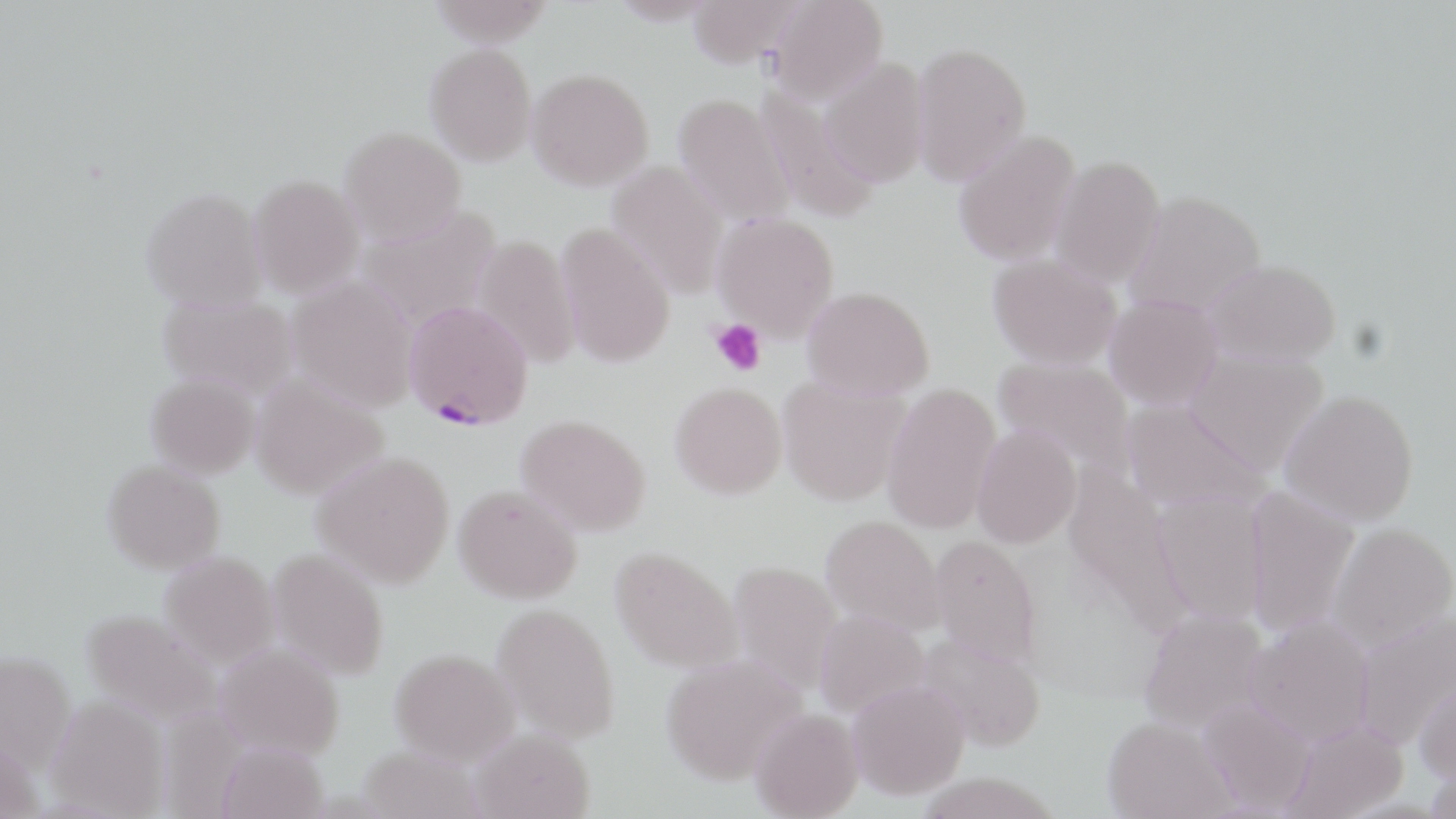 Approximate bounding boxes as [x1, y1, x2, y2] in pixels. Uninfected red blood cell locations: [427, 0, 557, 46], [686, 0, 806, 67], [765, 0, 888, 107], [910, 41, 1032, 185], [425, 43, 537, 166], [820, 58, 931, 188], [527, 68, 654, 191], [755, 87, 879, 224], [673, 93, 796, 230], [339, 126, 465, 245], [952, 130, 1081, 267], [1049, 155, 1165, 289], [608, 161, 729, 300], [248, 174, 364, 298], [141, 187, 268, 312], [1123, 189, 1266, 318], [357, 206, 500, 330], [712, 212, 839, 340], [555, 222, 676, 369], [472, 234, 581, 369], [988, 253, 1122, 370], [1203, 259, 1341, 367], [286, 275, 419, 412], [801, 285, 935, 399], [1104, 294, 1223, 410], [157, 295, 299, 400], [1183, 350, 1329, 475], [992, 356, 1137, 479], [145, 373, 259, 479], [250, 374, 388, 500], [777, 375, 910, 506], [669, 381, 787, 499], [882, 383, 1001, 534], [1280, 390, 1419, 525], [1120, 399, 1271, 515], [516, 414, 651, 537], [972, 425, 1081, 548], [312, 450, 455, 588], [102, 460, 226, 574], [1063, 464, 1192, 637], [453, 484, 582, 604], [1243, 487, 1359, 639], [1152, 490, 1270, 628], [821, 515, 945, 635], [1328, 524, 1456, 650], [930, 535, 1042, 667], [610, 546, 743, 673], [267, 548, 389, 680], [159, 551, 280, 669], [728, 561, 843, 695], [492, 603, 620, 743], [79, 608, 224, 729], [1354, 608, 1456, 749], [814, 609, 929, 717], [1138, 609, 1269, 735], [1245, 616, 1375, 746], [917, 631, 1046, 752], [213, 642, 345, 760], [389, 648, 520, 766], [0, 650, 77, 776], [660, 652, 807, 785], [1414, 674, 1456, 788], [846, 680, 970, 800], [46, 695, 170, 817], [1197, 699, 1317, 816], [750, 708, 864, 818], [1102, 716, 1236, 819], [1280, 721, 1408, 819], [470, 728, 595, 819], [214, 740, 330, 819], [357, 744, 487, 818]. Plasmodium falciparum-infected red blood cell locations: [403, 299, 533, 430]. Platelet locations: [711, 318, 766, 377]. Slide-level diagnosis: Plasmodium falciparum. Image is 1456×819 pixels. Light microscopy. One field of a larger specimen. 1000x magnification. Thin blood smear. May-Grünwald-Giemsa stain.